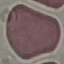
Summary:
  - Malaria status: uninfected
  - Capture: smartphone through the microscope eyepiece
  - Image type: cell patch, automatically extracted from a larger field of view and resized to 64 × 64 pixels
  - Preparation: thin smear
  - Stain: Giemsa